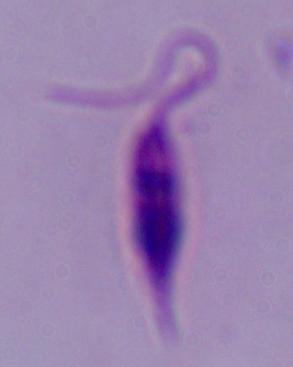

modality = micrograph
magnification = 1000x
identification = Leishmania